Report the malaria status of this cell.
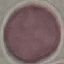
It is uninfected.

Summary:
  - Capture: smartphone through the microscope eyepiece
  - Image type: automatically extracted cell patch, resized to 64 × 64 pixels
  - Stain: Giemsa
  - Preparation: thin blood smear